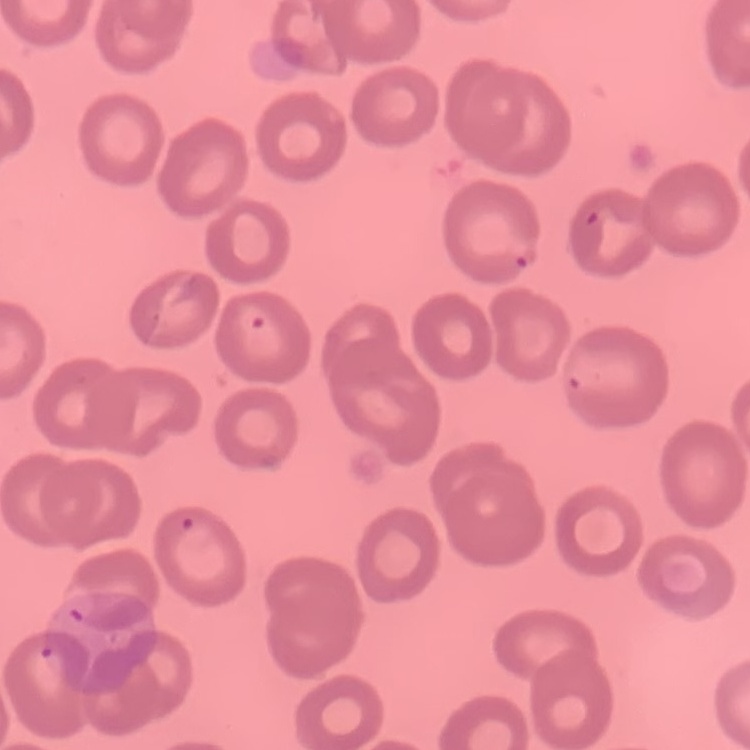

erythrocyte morphology = no rouleaux formation
stain = Field's or Giemsa
preparation = thin blood smear
image type = square crop of a larger photomicrograph